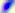 Toxoplasma gondii is shown. Micrograph. 400x magnification.